Report the malaria status of this cell.
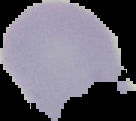

Uninfected.

Segmented cell region on a black background. From a thin blood smear. Image is 136×121 pixels.